Assess this cell for malaria.
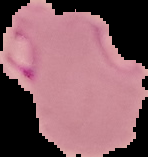

It is parasitized.

image type = segmented cell region with the area outside set to black
image size = 148×157 pixels
preparation = thin blood film